Assess this cell for malaria.
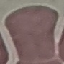
Uninfected.

preparation = thin blood film
image type = cell patch, automatically extracted from a larger field of view and resized to 64 × 64 pixels
capture = smartphone camera at the microscope eyepiece
stain = Giemsa